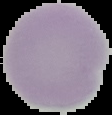

malaria status = uninfected
preparation = thin blood smear
image size = 112×115 pixels
image type = segmented cell region on a black background